Identify the parasite.
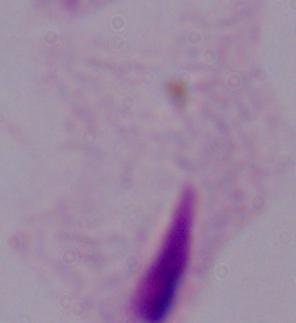
A trichomonad.

1000x magnification. Micrograph.